Comment on the morphology of the red blood cells.
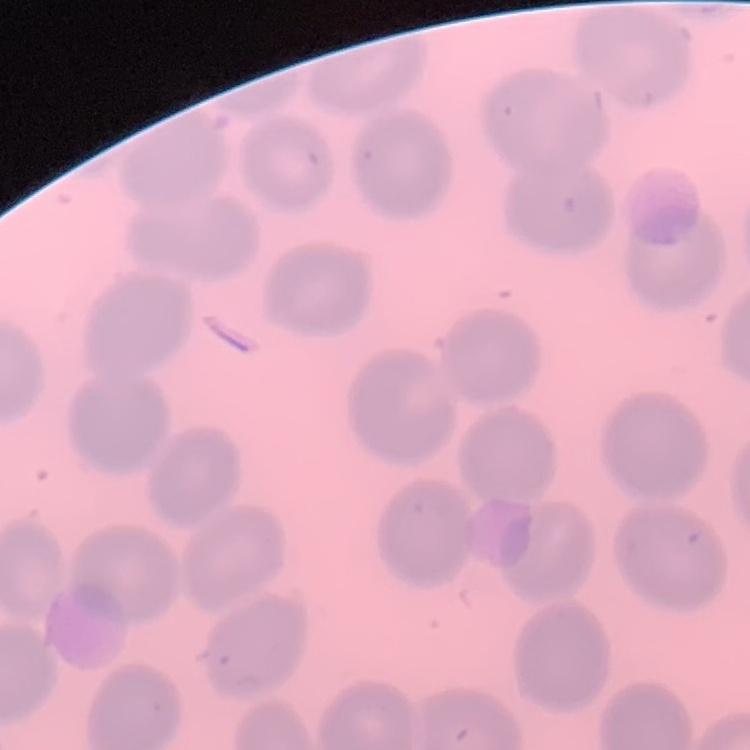
No rouleaux formation.

Thin peripheral smear. Square crop of a larger photomicrograph. Stained with either Field's or Giemsa.